Evaluate for malaria.
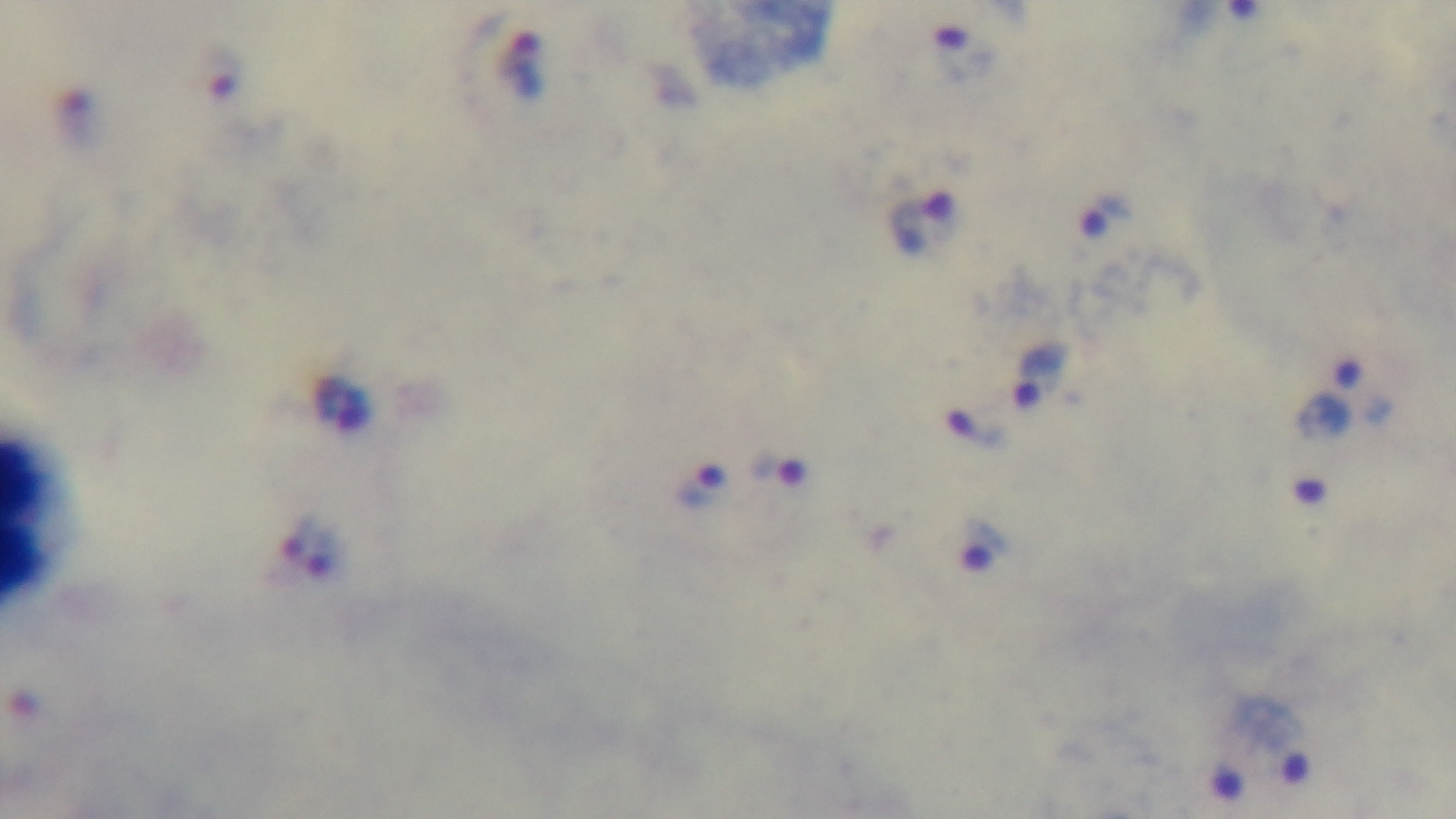

Infected.

Summary:
  - Field of view: single
  - Objective: 100x oil immersion
  - Capture: mounted 4K digital camera
  - Stain: Giemsa
  - Preparation: thick
  - Modality: light microscopy